Identify the parasite.
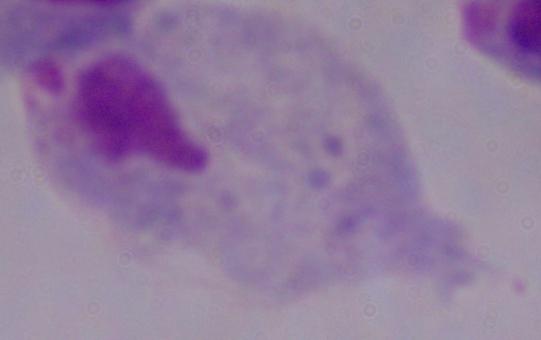

This is a trichomonad.

modality = micrograph
magnification = 1000x